Comment on the morphology of the erythrocytes.
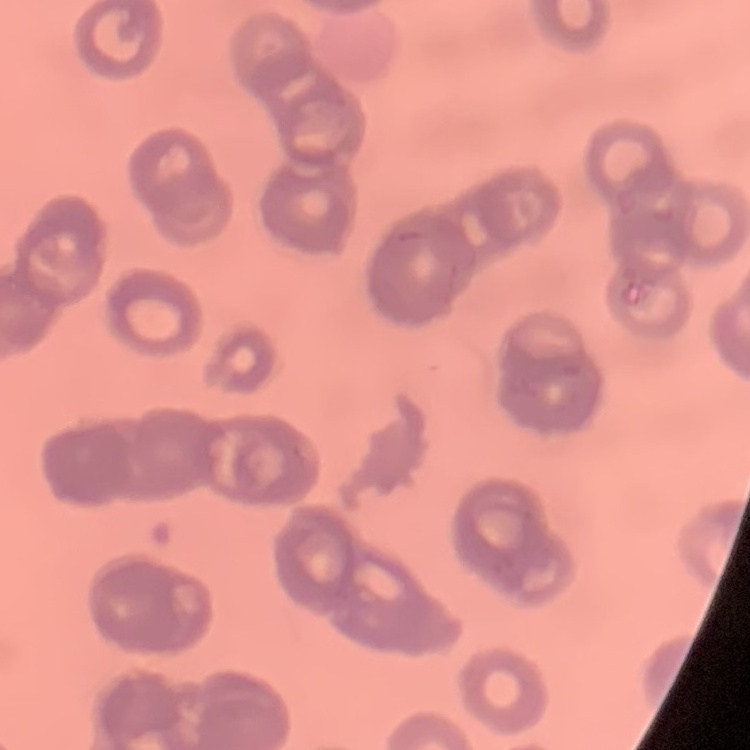

Rouleaux formation.

Field's or Giemsa stain. Thin peripheral smear. Square crop of a larger photomicrograph.